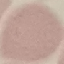

{
  "malaria_status": "uninfected",
  "image_type": "cell patch, automatically extracted from a larger field of view and resized to 64 × 64 pixels",
  "preparation": "thin smear",
  "stain": "Giemsa",
  "capture": "smartphone camera at the microscope eyepiece"
}